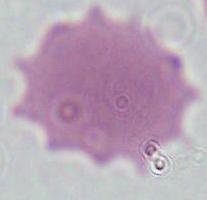
Photomicrograph. Captured at 1000x magnification. A red blood cell is seen.